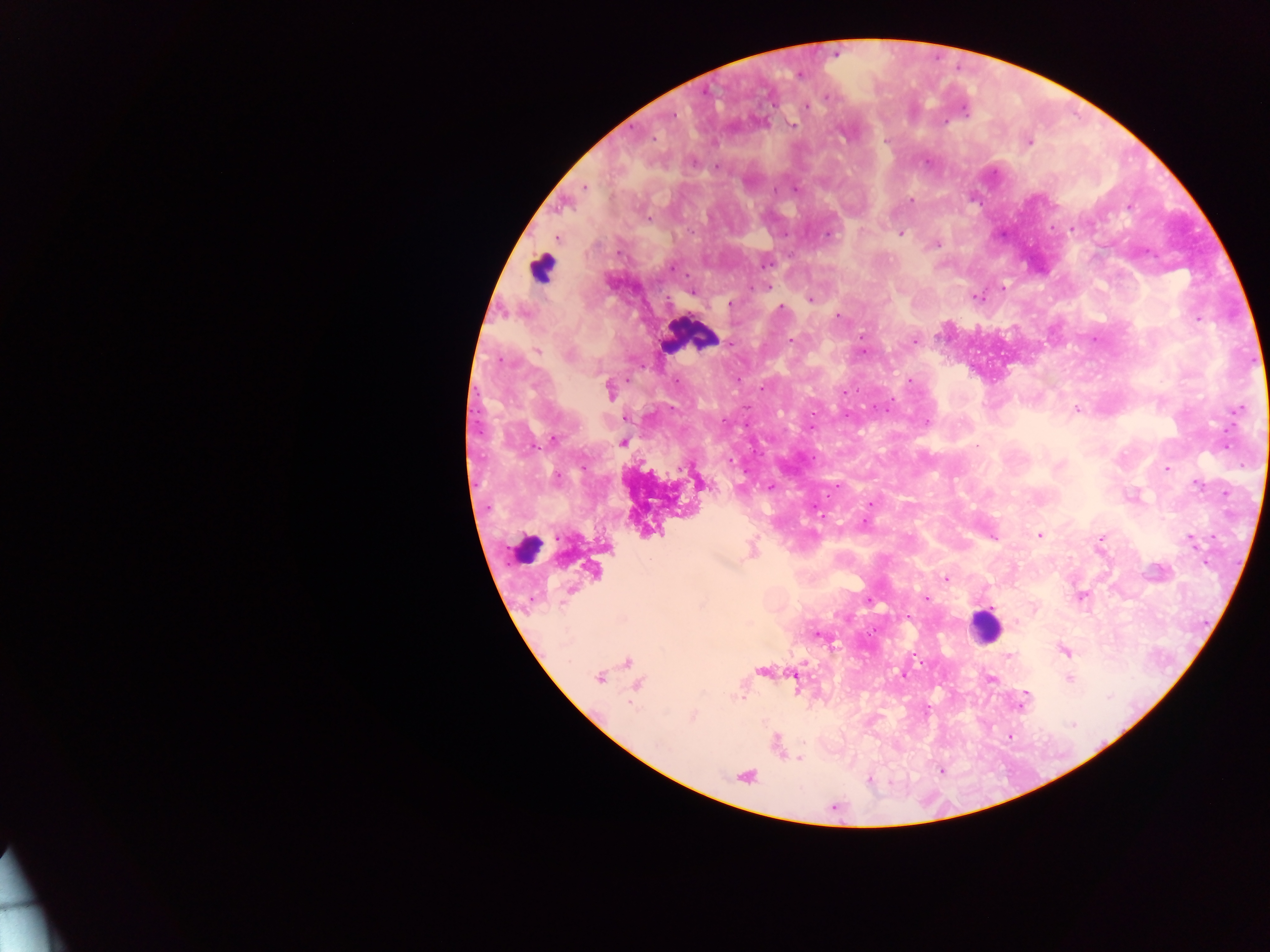

capture: mobile-phone photograph through a microscope
country: Ghana
plasmodium_parasite_locations: 'approximate centers as {x, y} in pixels: {800, 74}, {827, 96}, {806, 107}, {964, 111}, {673, 115}, {793, 125}, {884, 140}, {1029, 143}, {694, 162}, {717, 167}, {585, 188}, {795, 189}, {911, 200}, {1130, 207}, {648, 220}, {1070, 229}, {901, 235}, {827, 236}, {937, 246}, {766, 264}, {671, 268}, {768, 287}, {1003, 287}, {752, 288}, {692, 291}, {978, 297}, {809, 299}, {729, 304}, {781, 307}, {837, 316}, {1198, 320}, {861, 337}, {792, 340}, {914, 341}, {730, 343}, {538, 350}, {864, 352}, {568, 355}, {504, 362}, {910, 380}, {676, 382}, {762, 389}, {610, 390}, {844, 392}, {886, 409}, {1077, 410}, {1237, 410}, {812, 413}, {724, 421}, {928, 421}, {555, 438}, {623, 443}, {976, 445}, {1225, 446}, {730, 461}, {1167, 469}, {557, 477}, {1197, 485}, {770, 487}, {871, 504}, {864, 523}, {1040, 536}, {994, 537}, {1101, 538}, {1191, 541}, {946, 579}, {1080, 596}, {926, 599}, {870, 601}, {819, 635}, {1065, 652}, {1008, 656}, {904, 675}, {599, 678}, {991, 678}, {1069, 679}, {1026, 693}, {742, 698}, {1023, 699}, {1022, 705}, {693, 715}, {1073, 724}, {799, 760}'
image_size: 1270×952 pixels
leukocyte_locations: 'approximate centers as {x, y} in pixels: {542, 268}, {691, 335}, {526, 546}, {985, 626}'
field_of_view: single
preparation: thick blood film